Comment on the morphology of the red blood cells.
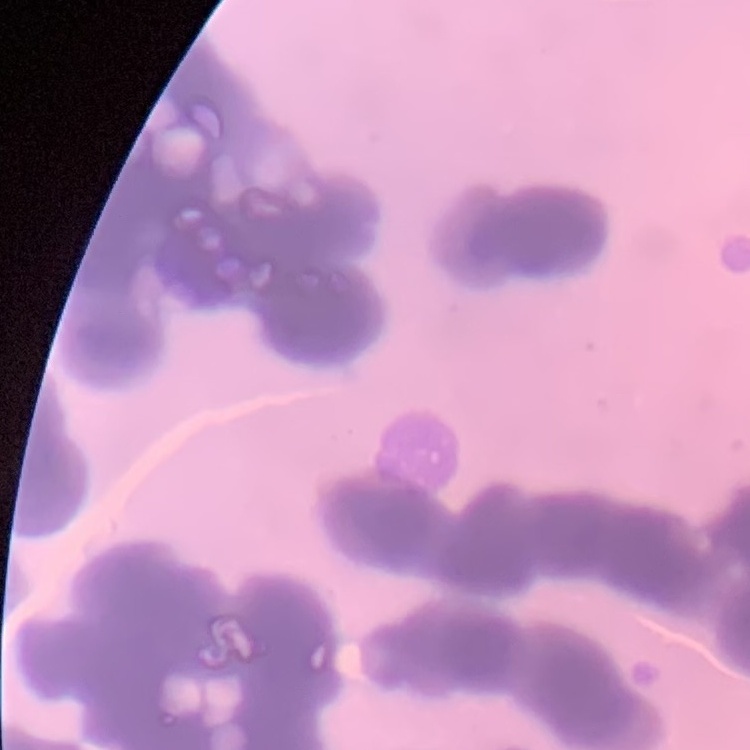
Rouleaux formation.

One tile cut from a larger photomicrograph. Thin blood smear. Field's or Giemsa stain.